Locate leukocytes (white blood cells).
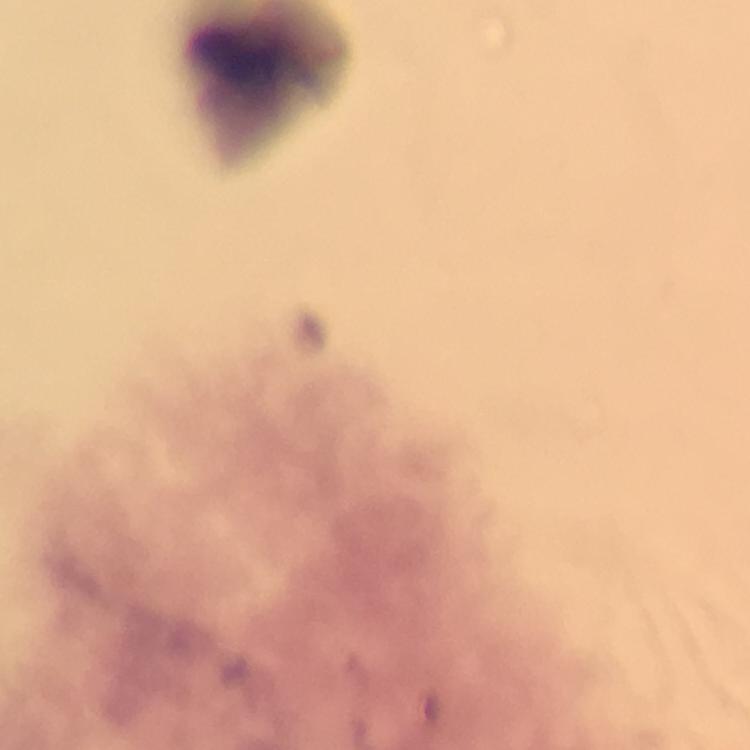

Approximate centers as {x, y} in pixels.
Leukocytes: {261, 69}.

Image is 750×750 pixels. From a diagnostic examination for malaria. At 100x magnification. Smartphone photograph taken through a microscope. A crop from one field of view. Plasmodium parasites: none detected. Giemsa stain. Immersion oil was used. Thick blood smear.